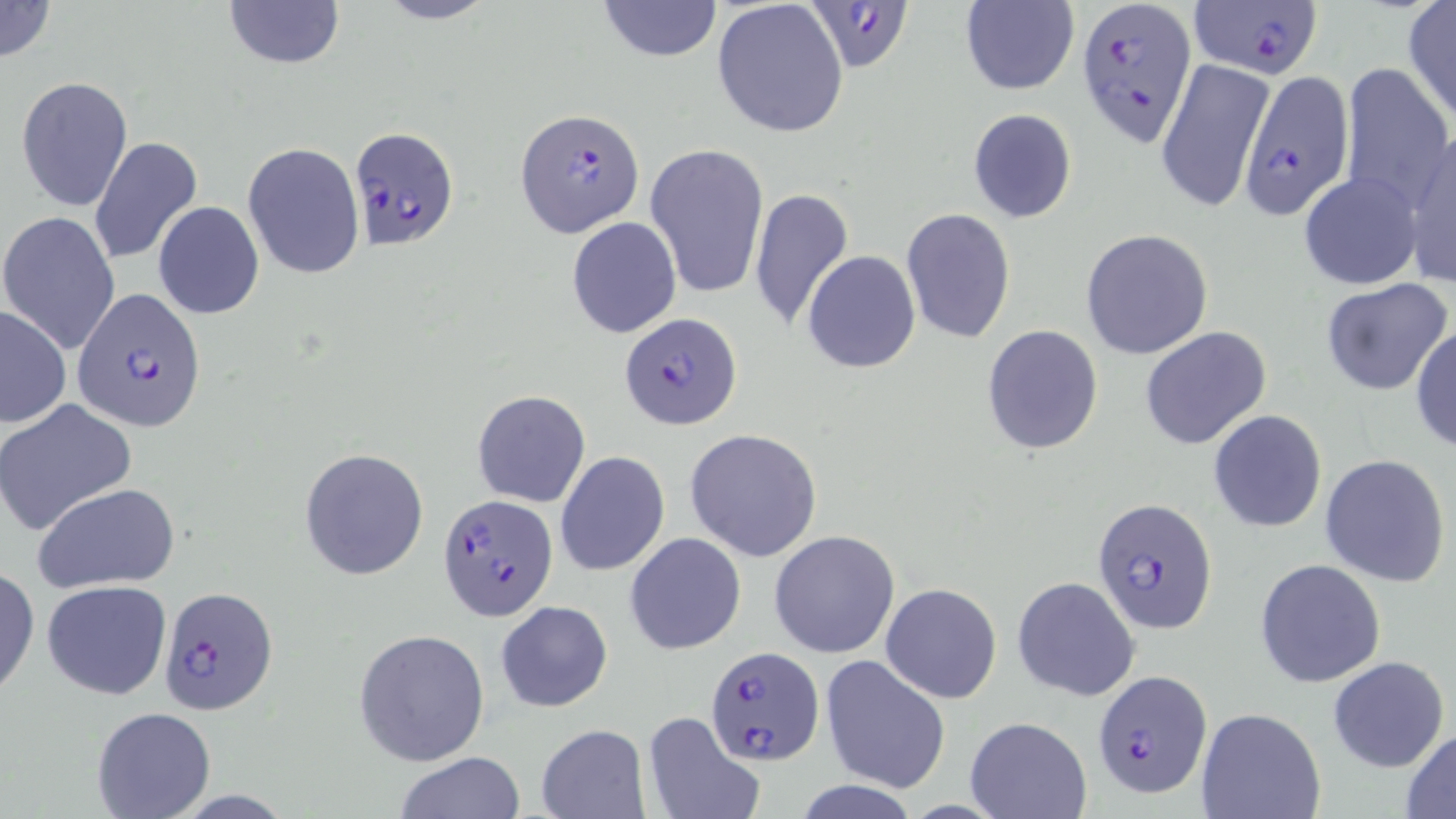
Summary:
  - Coordinate format: approximate bounding boxes as named x1/y1/x2/y2 corners in pixels
  - Uninfected red blood cell locations: (x1=0, y1=0, x2=56, y2=63), (x1=222, y1=0, x2=344, y2=70), (x1=375, y1=0, x2=497, y2=25), (x1=599, y1=0, x2=721, y2=62), (x1=711, y1=0, x2=850, y2=139), (x1=958, y1=2, x2=1079, y2=95), (x1=1401, y1=3, x2=1456, y2=126), (x1=1157, y1=57, x2=1276, y2=214), (x1=1337, y1=63, x2=1452, y2=209), (x1=17, y1=76, x2=133, y2=214), (x1=967, y1=108, x2=1078, y2=224), (x1=1404, y1=132, x2=1456, y2=289), (x1=89, y1=136, x2=203, y2=267), (x1=646, y1=140, x2=768, y2=302), (x1=242, y1=142, x2=364, y2=279), (x1=1299, y1=172, x2=1423, y2=291), (x1=748, y1=187, x2=854, y2=331), (x1=154, y1=201, x2=264, y2=319), (x1=902, y1=208, x2=1015, y2=343), (x1=1, y1=212, x2=122, y2=355), (x1=566, y1=216, x2=682, y2=339), (x1=807, y1=227, x2=1013, y2=358), (x1=1081, y1=229, x2=1214, y2=360), (x1=802, y1=250, x2=921, y2=373), (x1=1320, y1=277, x2=1452, y2=396), (x1=0, y1=306, x2=71, y2=427), (x1=1411, y1=323, x2=1456, y2=452), (x1=981, y1=325, x2=1104, y2=454), (x1=1139, y1=326, x2=1273, y2=450), (x1=473, y1=390, x2=590, y2=507), (x1=0, y1=398, x2=137, y2=536), (x1=1208, y1=409, x2=1327, y2=534), (x1=685, y1=429, x2=823, y2=561), (x1=299, y1=447, x2=430, y2=581), (x1=556, y1=451, x2=669, y2=576), (x1=1320, y1=454, x2=1451, y2=587), (x1=33, y1=482, x2=181, y2=593), (x1=769, y1=530, x2=900, y2=659), (x1=625, y1=532, x2=746, y2=655), (x1=1254, y1=558, x2=1385, y2=688), (x1=0, y1=566, x2=39, y2=701), (x1=1013, y1=575, x2=1140, y2=702), (x1=42, y1=580, x2=171, y2=701), (x1=881, y1=583, x2=1003, y2=704), (x1=496, y1=599, x2=613, y2=713), (x1=353, y1=629, x2=490, y2=766), (x1=821, y1=655, x2=948, y2=793), (x1=1326, y1=655, x2=1449, y2=773), (x1=92, y1=705, x2=215, y2=817), (x1=1196, y1=709, x2=1326, y2=819), (x1=642, y1=711, x2=763, y2=819), (x1=964, y1=715, x2=1092, y2=819), (x1=536, y1=724, x2=650, y2=818), (x1=1401, y1=728, x2=1456, y2=817), (x1=394, y1=752, x2=525, y2=819), (x1=793, y1=780, x2=921, y2=817)
  - Plasmodium falciparum-infected red blood cell locations: (x1=804, y1=0, x2=910, y2=73), (x1=1078, y1=0, x2=1198, y2=146), (x1=1189, y1=0, x2=1324, y2=74), (x1=1237, y1=66, x2=1360, y2=217), (x1=515, y1=109, x2=645, y2=238), (x1=346, y1=126, x2=459, y2=251), (x1=74, y1=290, x2=206, y2=429), (x1=619, y1=312, x2=741, y2=429), (x1=438, y1=494, x2=557, y2=621), (x1=1093, y1=498, x2=1217, y2=633), (x1=157, y1=585, x2=278, y2=718), (x1=705, y1=649, x2=824, y2=766), (x1=1095, y1=670, x2=1213, y2=799)
  - Slide-level diagnosis: Plasmodium falciparum
  - Field of view: one of a larger specimen
  - Preparation: thin blood smear
  - Image size: 1456×819 pixels
  - Magnification: 1000x
  - Stain: May-Grünwald-Giemsa
  - Modality: optical microscopy